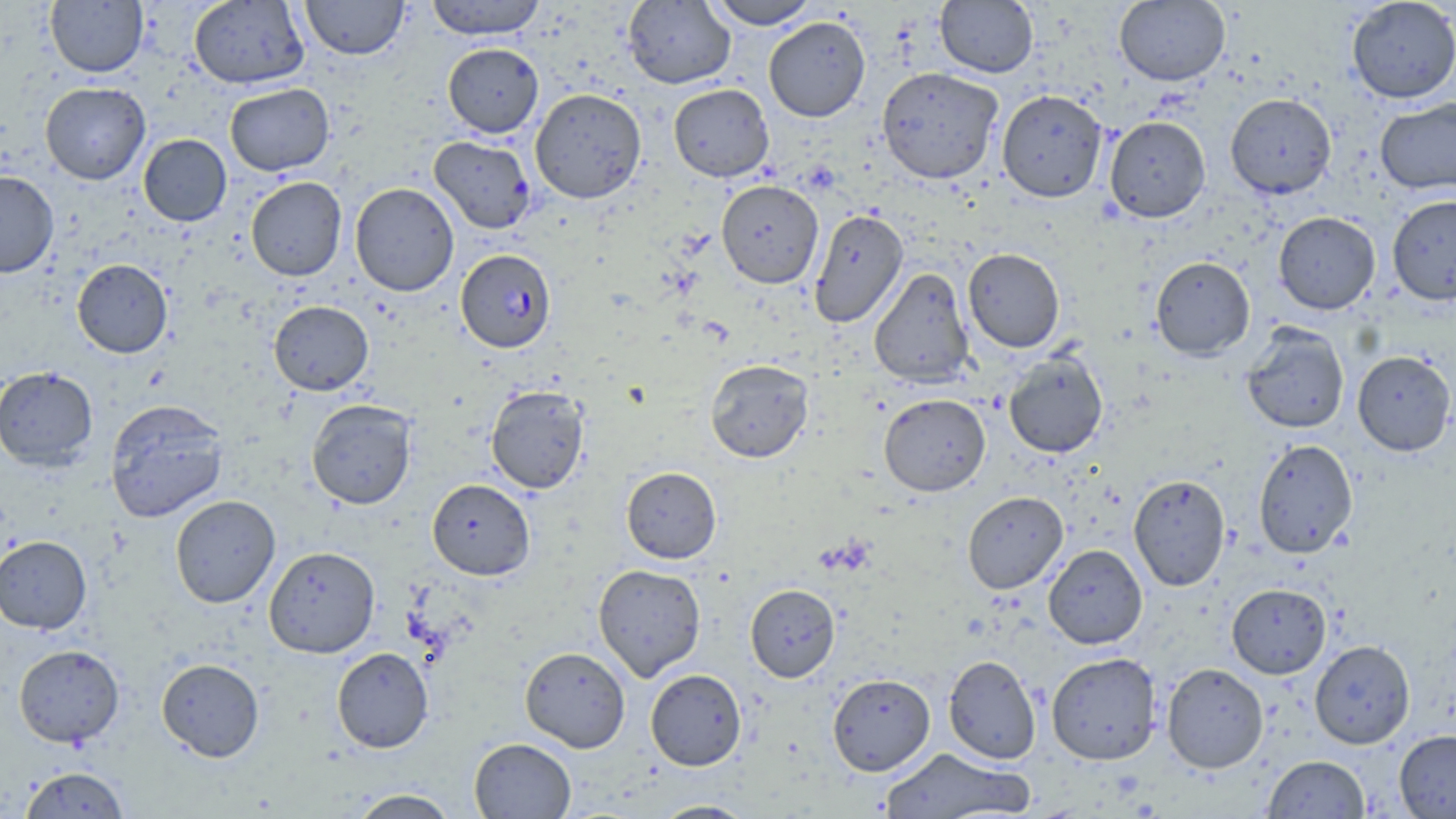
slide_level_diagnosis: Plasmodium falciparum
uninfected_red_blood_cell_locations: 'approximate bounding boxes as (x1,y1)-(x2,y2) corner pairs in pixels: (189,0)-(309,89), (300,0)-(409,59), (424,0)-(548,39), (705,0)-(820,29), (1346,0)-(1456,103), (45,1)-(148,77), (623,1)-(735,89), (935,1)-(1038,77), (1115,1)-(1230,85), (763,16)-(871,121), (443,43)-(543,138), (877,66)-(1004,183), (40,82)-(150,184), (224,83)-(334,176), (668,83)-(774,182), (530,88)-(646,203), (997,89)-(1108,202), (1225,93)-(1336,199), (1375,97)-(1456,195), (1104,116)-(1211,222), (138,134)-(231,226), (429,136)-(536,233), (0,170)-(59,277), (245,176)-(347,281), (716,179)-(824,288), (349,182)-(459,296), (1387,195)-(1456,305), (809,209)-(908,328), (1273,211)-(1380,314), (963,248)-(1065,353), (1150,256)-(1255,360), (72,259)-(173,358), (869,267)-(974,388), (269,300)-(373,395), (1241,324)-(1350,434), (1004,350)-(1108,458), (1352,350)-(1455,456), (705,359)-(813,462), (0,365)-(98,470), (486,384)-(589,494), (879,393)-(990,496), (105,399)-(229,522), (307,399)-(417,509), (1253,439)-(1359,558), (621,466)-(721,563), (1128,474)-(1230,591), (426,478)-(535,580), (962,491)-(1068,594), (170,494)-(280,607), (0,535)-(92,634), (1043,544)-(1147,649), (264,545)-(380,658), (593,564)-(706,682), (745,583)-(840,682), (1227,583)-(1331,678), (1309,639)-(1415,749), (13,644)-(124,747), (520,646)-(631,753), (331,647)-(434,753), (1046,652)-(1161,765), (943,654)-(1041,764), (156,658)-(265,762), (1162,662)-(1269,773), (645,668)-(747,770), (827,673)-(935,776), (1394,729)-(1456,818), (469,737)-(576,818), (878,747)-(1034,819), (1262,755)-(1370,818), (20,766)-(130,818), (348,788)-(459,818), (651,800)-(757,818)'
plasmodium_falciparum_infected_red_blood_cell_locations: 'approximate bounding boxes as (x1,y1)-(x2,y2) corner pairs in pixels: (456,249)-(556,352)'
preparation: thin blood smear
image_size: 1456×819 pixels
modality: optical microscopy
magnification: 1000x
field_of_view: single
stain: May-Grünwald-Giemsa